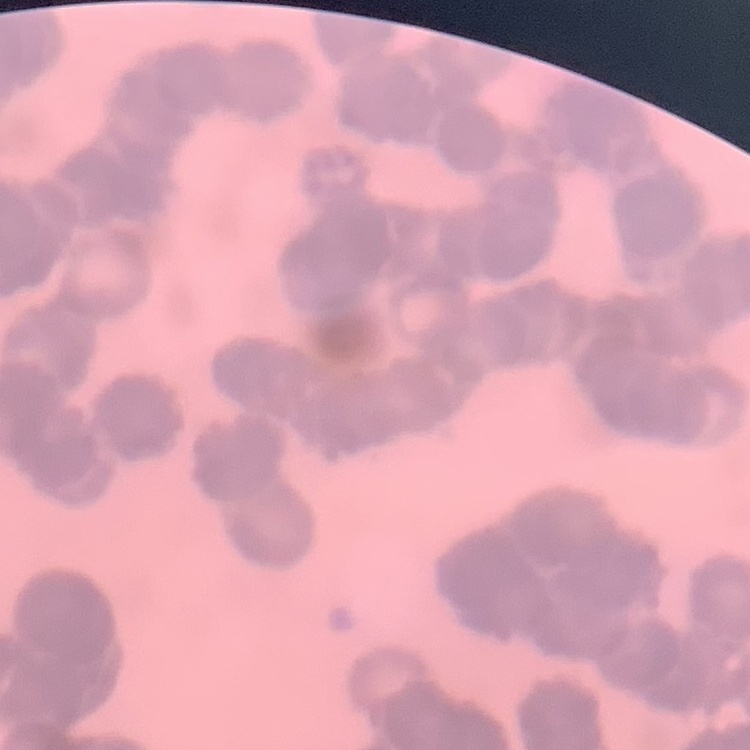

red_blood_cell_morphology: rouleaux formation
stain: Field's or Giemsa
preparation: thin blood smear
image_type: square crop of a larger photomicrograph